Outline each Plasmodium falciparum-infected red blood cell.
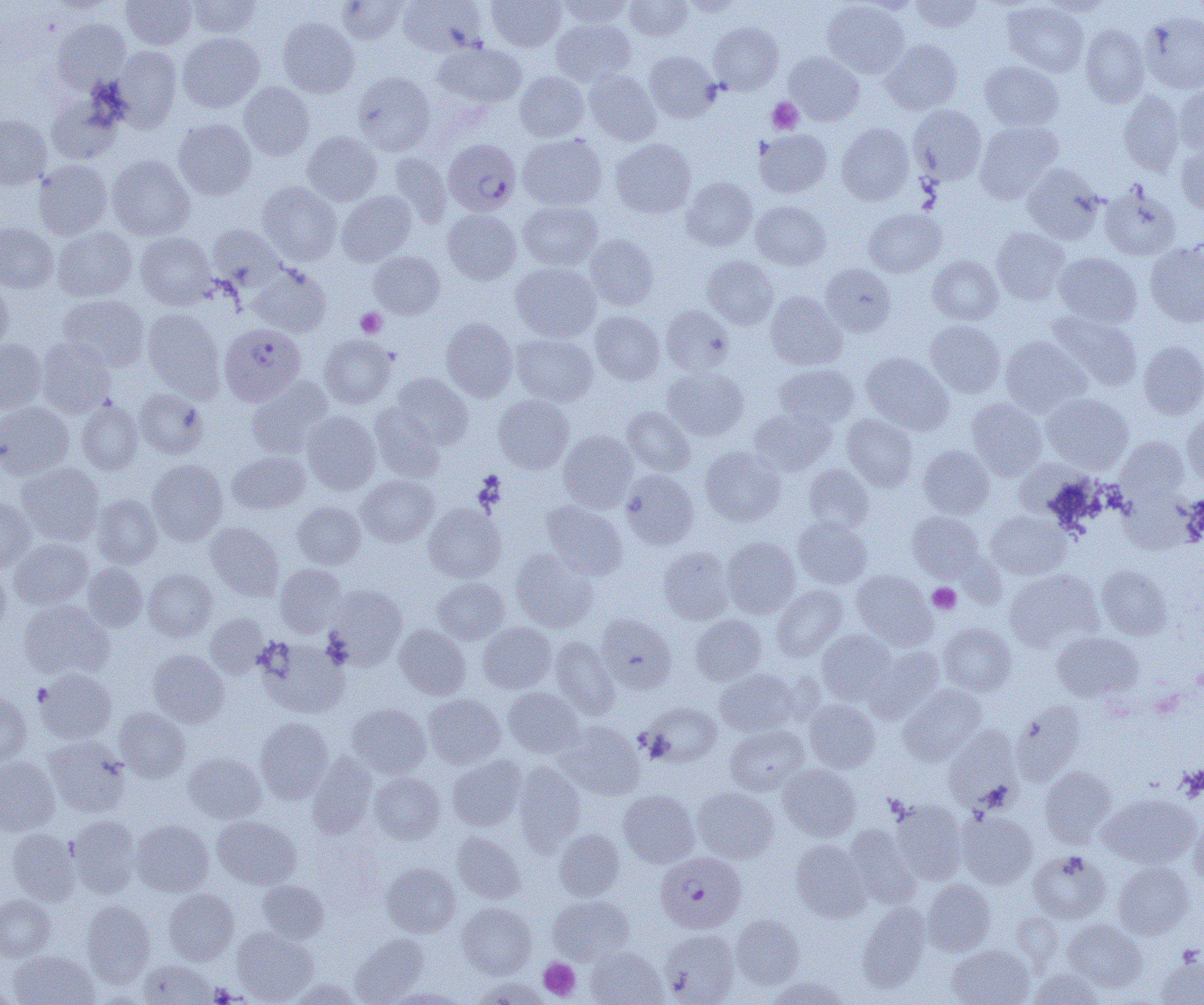
Approximate bounding boxes as named x1/y1/x2/y2 corners in pixels.
Plasmodium falciparum-infected red blood cells: (x1=443, y1=139, x2=521, y2=216), (x1=219, y1=323, x2=305, y2=406), (x1=656, y1=854, x2=748, y2=932).

slide-level diagnosis = Plasmodium falciparum
modality = light microscopy
image size = 1204×1005 pixels
magnification = 1000x
uninfected red blood cell locations = approximate bounding boxes as named x1/y1/x2/y2 corners in pixels: (x1=121, y1=0, x2=196, y2=50), (x1=185, y1=0, x2=261, y2=39), (x1=336, y1=0, x2=409, y2=45), (x1=487, y1=0, x2=565, y2=51), (x1=558, y1=0, x2=633, y2=29), (x1=624, y1=0, x2=694, y2=41), (x1=910, y1=0, x2=983, y2=32), (x1=1042, y1=0, x2=1112, y2=17), (x1=398, y1=1, x2=487, y2=56), (x1=822, y1=1, x2=909, y2=78), (x1=1003, y1=2, x2=1088, y2=77), (x1=1140, y1=11, x2=1204, y2=94), (x1=278, y1=17, x2=359, y2=98), (x1=52, y1=19, x2=130, y2=94), (x1=551, y1=19, x2=636, y2=87), (x1=709, y1=22, x2=783, y2=95), (x1=1080, y1=24, x2=1149, y2=107), (x1=177, y1=32, x2=264, y2=113), (x1=881, y1=39, x2=962, y2=115), (x1=434, y1=43, x2=527, y2=108), (x1=112, y1=46, x2=182, y2=131), (x1=644, y1=51, x2=720, y2=123), (x1=784, y1=52, x2=864, y2=126), (x1=980, y1=61, x2=1063, y2=131), (x1=584, y1=70, x2=661, y2=146), (x1=353, y1=71, x2=436, y2=156), (x1=515, y1=71, x2=589, y2=141), (x1=239, y1=82, x2=314, y2=161), (x1=1174, y1=86, x2=1204, y2=157), (x1=1118, y1=90, x2=1185, y2=176), (x1=46, y1=92, x2=124, y2=164), (x1=908, y1=104, x2=987, y2=185), (x1=0, y1=115, x2=51, y2=189), (x1=173, y1=119, x2=257, y2=200), (x1=974, y1=121, x2=1063, y2=203), (x1=836, y1=123, x2=914, y2=205), (x1=755, y1=129, x2=831, y2=197), (x1=302, y1=131, x2=382, y2=206), (x1=517, y1=134, x2=607, y2=210), (x1=610, y1=138, x2=696, y2=218), (x1=1176, y1=144, x2=1204, y2=213), (x1=388, y1=152, x2=452, y2=229), (x1=107, y1=154, x2=195, y2=241), (x1=34, y1=159, x2=113, y2=240), (x1=1022, y1=164, x2=1106, y2=245), (x1=681, y1=177, x2=757, y2=251), (x1=257, y1=181, x2=341, y2=266), (x1=1099, y1=183, x2=1181, y2=260), (x1=336, y1=190, x2=416, y2=266), (x1=518, y1=201, x2=603, y2=271), (x1=751, y1=201, x2=830, y2=270), (x1=863, y1=208, x2=946, y2=278), (x1=443, y1=209, x2=521, y2=284), (x1=0, y1=223, x2=58, y2=293), (x1=207, y1=224, x2=287, y2=290), (x1=52, y1=227, x2=138, y2=301), (x1=992, y1=228, x2=1070, y2=305), (x1=136, y1=232, x2=216, y2=310), (x1=585, y1=234, x2=658, y2=309), (x1=1145, y1=241, x2=1204, y2=328), (x1=368, y1=251, x2=445, y2=318), (x1=1054, y1=252, x2=1141, y2=328), (x1=702, y1=256, x2=778, y2=330), (x1=927, y1=256, x2=1003, y2=325), (x1=511, y1=262, x2=601, y2=342), (x1=821, y1=263, x2=896, y2=337), (x1=247, y1=264, x2=331, y2=337), (x1=0, y1=279, x2=13, y2=354), (x1=765, y1=291, x2=847, y2=370), (x1=58, y1=294, x2=150, y2=371), (x1=660, y1=305, x2=734, y2=377), (x1=142, y1=308, x2=225, y2=401), (x1=590, y1=311, x2=665, y2=385), (x1=1046, y1=311, x2=1142, y2=392), (x1=441, y1=318, x2=518, y2=401), (x1=925, y1=320, x2=1005, y2=398), (x1=511, y1=334, x2=598, y2=406), (x1=319, y1=335, x2=396, y2=409), (x1=1000, y1=336, x2=1091, y2=416), (x1=36, y1=337, x2=116, y2=417), (x1=0, y1=339, x2=47, y2=415), (x1=1138, y1=340, x2=1204, y2=419), (x1=861, y1=352, x2=953, y2=435), (x1=774, y1=363, x2=859, y2=428), (x1=662, y1=367, x2=749, y2=441), (x1=391, y1=373, x2=474, y2=449), (x1=246, y1=376, x2=333, y2=459), (x1=133, y1=388, x2=208, y2=459), (x1=1042, y1=393, x2=1133, y2=474), (x1=493, y1=395, x2=574, y2=474), (x1=966, y1=397, x2=1047, y2=480), (x1=77, y1=400, x2=143, y2=475), (x1=0, y1=402, x2=74, y2=479), (x1=369, y1=403, x2=444, y2=483), (x1=622, y1=407, x2=695, y2=476), (x1=750, y1=407, x2=836, y2=475), (x1=1182, y1=410, x2=1204, y2=486), (x1=302, y1=411, x2=380, y2=495), (x1=842, y1=414, x2=918, y2=491), (x1=558, y1=430, x2=637, y2=513), (x1=1117, y1=437, x2=1189, y2=504), (x1=919, y1=445, x2=994, y2=518), (x1=700, y1=446, x2=785, y2=526), (x1=228, y1=451, x2=310, y2=514), (x1=147, y1=459, x2=228, y2=546), (x1=17, y1=462, x2=104, y2=545), (x1=804, y1=464, x2=874, y2=534), (x1=621, y1=470, x2=699, y2=549), (x1=356, y1=475, x2=438, y2=547), (x1=1119, y1=489, x2=1196, y2=555), (x1=91, y1=494, x2=162, y2=568), (x1=0, y1=498, x2=35, y2=572), (x1=541, y1=500, x2=627, y2=580), (x1=292, y1=502, x2=365, y2=569), (x1=424, y1=503, x2=506, y2=583), (x1=986, y1=510, x2=1070, y2=579), (x1=907, y1=511, x2=984, y2=580), (x1=793, y1=517, x2=872, y2=588), (x1=205, y1=522, x2=284, y2=601), (x1=722, y1=537, x2=800, y2=618), (x1=10, y1=538, x2=93, y2=609), (x1=658, y1=546, x2=734, y2=624), (x1=511, y1=548, x2=597, y2=633), (x1=83, y1=563, x2=147, y2=631), (x1=0, y1=564, x2=10, y2=635), (x1=275, y1=564, x2=347, y2=637), (x1=1097, y1=564, x2=1172, y2=640), (x1=143, y1=569, x2=217, y2=641), (x1=1004, y1=569, x2=1103, y2=652), (x1=852, y1=570, x2=936, y2=649), (x1=431, y1=577, x2=510, y2=644), (x1=325, y1=584, x2=407, y2=669), (x1=772, y1=584, x2=847, y2=661), (x1=19, y1=600, x2=113, y2=679), (x1=205, y1=613, x2=268, y2=678), (x1=596, y1=613, x2=676, y2=692), (x1=691, y1=615, x2=766, y2=685), (x1=478, y1=622, x2=556, y2=694), (x1=938, y1=622, x2=1016, y2=696), (x1=394, y1=624, x2=471, y2=699), (x1=817, y1=629, x2=896, y2=704), (x1=1052, y1=631, x2=1142, y2=702), (x1=550, y1=636, x2=619, y2=719), (x1=257, y1=637, x2=350, y2=718), (x1=865, y1=645, x2=944, y2=723), (x1=148, y1=649, x2=229, y2=728), (x1=35, y1=668, x2=117, y2=744), (x1=715, y1=669, x2=798, y2=736), (x1=898, y1=684, x2=987, y2=765), (x1=503, y1=687, x2=584, y2=758), (x1=0, y1=692, x2=32, y2=767), (x1=423, y1=693, x2=505, y2=769), (x1=805, y1=699, x2=879, y2=772), (x1=1011, y1=701, x2=1085, y2=785), (x1=642, y1=702, x2=722, y2=766), (x1=347, y1=703, x2=430, y2=778), (x1=115, y1=707, x2=190, y2=782), (x1=255, y1=717, x2=333, y2=803), (x1=557, y1=722, x2=645, y2=799), (x1=725, y1=725, x2=809, y2=795), (x1=944, y1=726, x2=1022, y2=812), (x1=44, y1=735, x2=130, y2=817), (x1=183, y1=752, x2=266, y2=823), (x1=307, y1=752, x2=378, y2=838), (x1=448, y1=754, x2=526, y2=831), (x1=0, y1=756, x2=59, y2=836), (x1=514, y1=762, x2=585, y2=852), (x1=778, y1=764, x2=860, y2=841), (x1=1040, y1=765, x2=1117, y2=848), (x1=369, y1=772, x2=445, y2=844), (x1=693, y1=787, x2=778, y2=862), (x1=619, y1=790, x2=699, y2=867), (x1=1099, y1=794, x2=1199, y2=868), (x1=890, y1=799, x2=967, y2=883), (x1=957, y1=810, x2=1037, y2=888), (x1=68, y1=815, x2=141, y2=898), (x1=1189, y1=815, x2=1204, y2=886), (x1=213, y1=816, x2=301, y2=889), (x1=131, y1=820, x2=213, y2=896), (x1=844, y1=824, x2=921, y2=908), (x1=7, y1=828, x2=81, y2=905), (x1=554, y1=829, x2=624, y2=901), (x1=452, y1=831, x2=525, y2=903), (x1=790, y1=839, x2=871, y2=922), (x1=1028, y1=850, x2=1110, y2=923), (x1=1113, y1=861, x2=1194, y2=939), (x1=381, y1=862, x2=460, y2=937), (x1=922, y1=879, x2=996, y2=955), (x1=259, y1=881, x2=328, y2=943), (x1=163, y1=888, x2=239, y2=965), (x1=0, y1=895, x2=54, y2=961), (x1=548, y1=895, x2=633, y2=964), (x1=82, y1=900, x2=155, y2=986), (x1=457, y1=902, x2=536, y2=978), (x1=857, y1=902, x2=931, y2=992), (x1=1012, y1=912, x2=1063, y2=970), (x1=731, y1=914, x2=805, y2=988), (x1=1062, y1=919, x2=1147, y2=992), (x1=232, y1=927, x2=317, y2=1004), (x1=660, y1=929, x2=739, y2=1004), (x1=351, y1=933, x2=428, y2=1004), (x1=947, y1=944, x2=1034, y2=1005), (x1=586, y1=946, x2=667, y2=1005), (x1=8, y1=950, x2=98, y2=1005), (x1=1156, y1=957, x2=1204, y2=1004), (x1=139, y1=959, x2=216, y2=1004), (x1=1028, y1=968, x2=1105, y2=1004), (x1=767, y1=976, x2=852, y2=1005), (x1=471, y1=977, x2=553, y2=1005), (x1=287, y1=978, x2=361, y2=1005), (x1=385, y1=988, x2=469, y2=1004)
preparation = thin blood film
platelet locations = approximate bounding boxes as named x1/y1/x2/y2 corners in pixels: (x1=767, y1=97, x2=803, y2=134), (x1=355, y1=308, x2=387, y2=338), (x1=928, y1=582, x2=961, y2=614), (x1=32, y1=684, x2=52, y2=706), (x1=1178, y1=766, x2=1204, y2=802), (x1=1176, y1=945, x2=1203, y2=967), (x1=538, y1=958, x2=580, y2=1000), (x1=209, y1=982, x2=237, y2=1004)
field of view = one of a larger specimen